Describe the morphology of the erythrocytes.
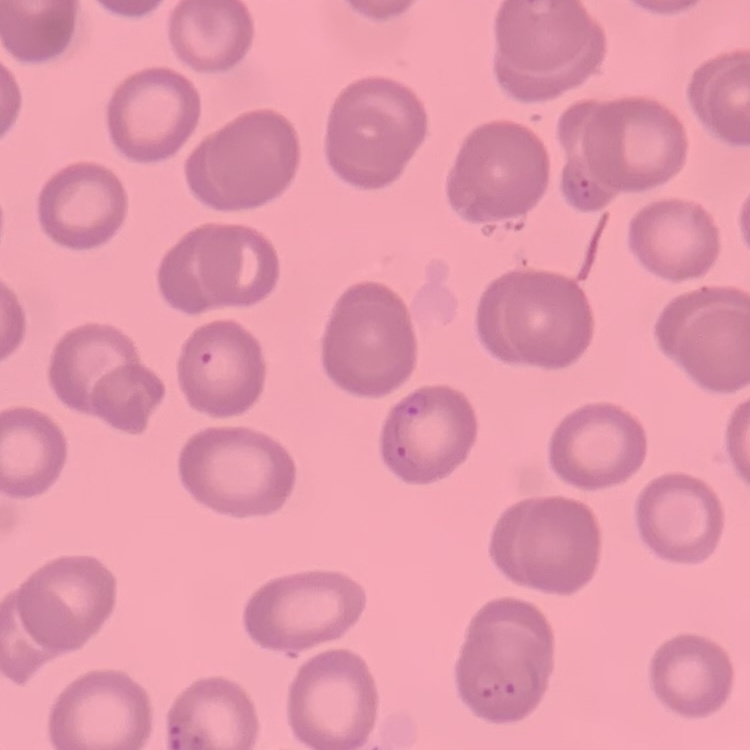

They show no rouleaux formation.

stain = Field's or Giemsa
preparation = thin blood smear
image type = square crop of a larger photomicrograph